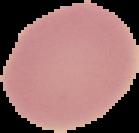

preparation: thin blood smear
image_size: 139×133 pixels
malaria_status: uninfected
image_type: segmented cell region on a black background